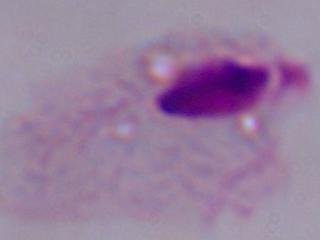
magnification = 1000x
identification = trichomonad
modality = photomicrograph